State which parasite is depicted.
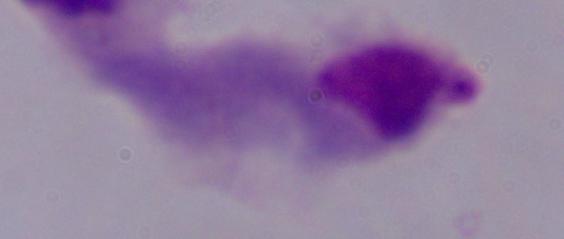

A trichomonad.

1000x magnification. Micrograph.